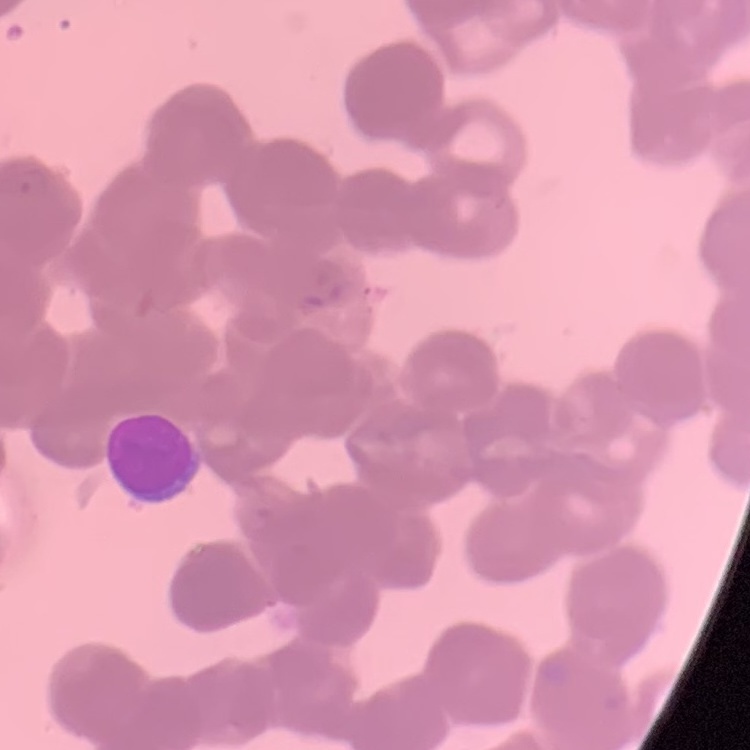
red_blood_cell_morphology: rouleaux formation
preparation: thin blood film
image_type: one tile cut from a larger photomicrograph
stain: Field's or Giemsa